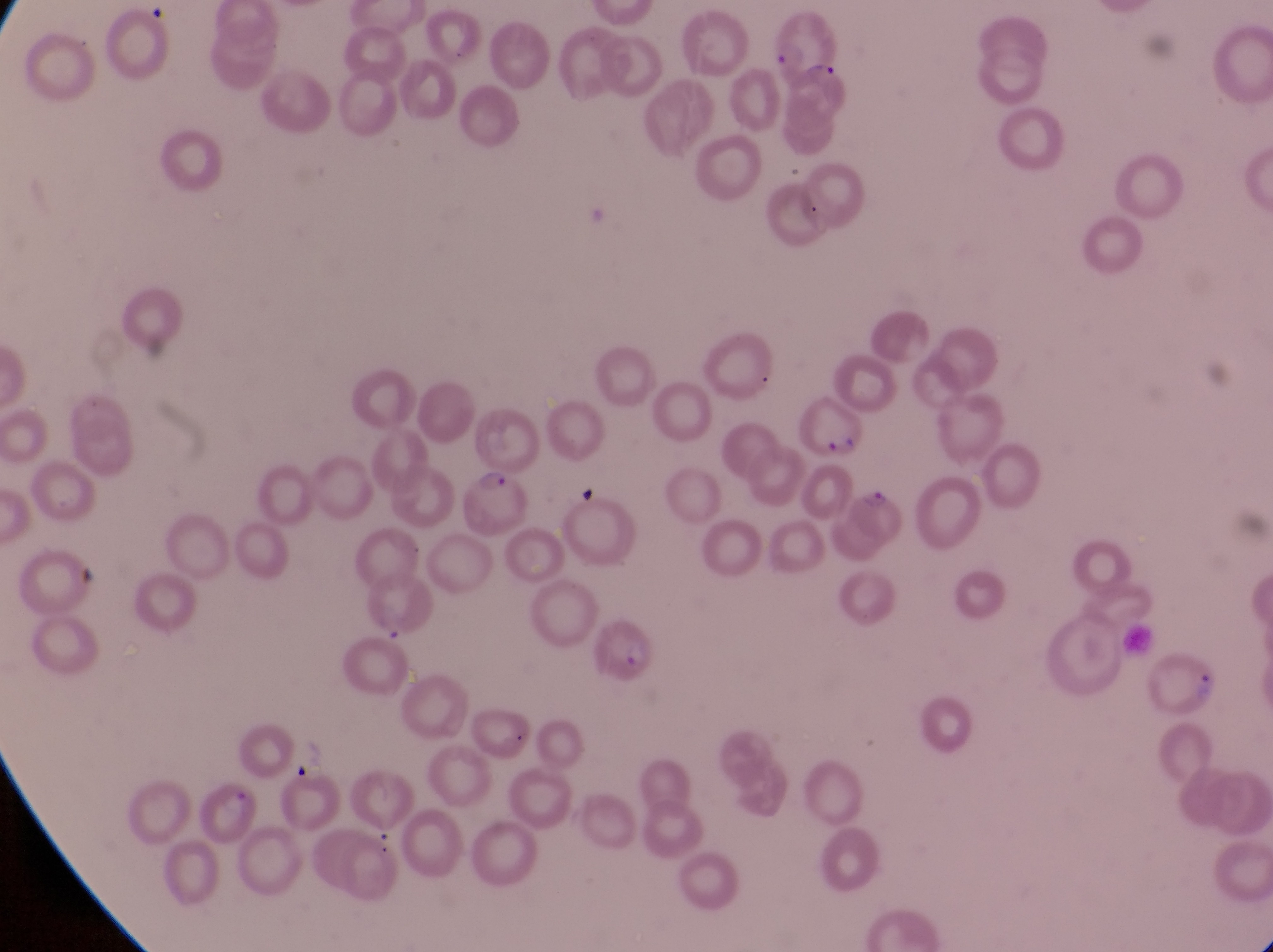
Approximate bounding boxes as [left, top, right, bottom] in pixels.
Summary:
  - Artifact (platelet-like body, stain precipitate, or debris) locations: [593, 623, 662, 686]
  - Parasitised red blood cell locations: [766, 15, 844, 77], [798, 394, 867, 462], [457, 464, 529, 538], [850, 485, 911, 548], [1145, 646, 1225, 721], [196, 781, 256, 841]
  - Field of view: single
  - Country: Uganda
  - Capture: smartphone photograph through the eyepiece of an Olympus CX-23 microscope
  - Preparation: thin blood film
  - Image size: 1273×952 pixels
  - Magnification: 1000x